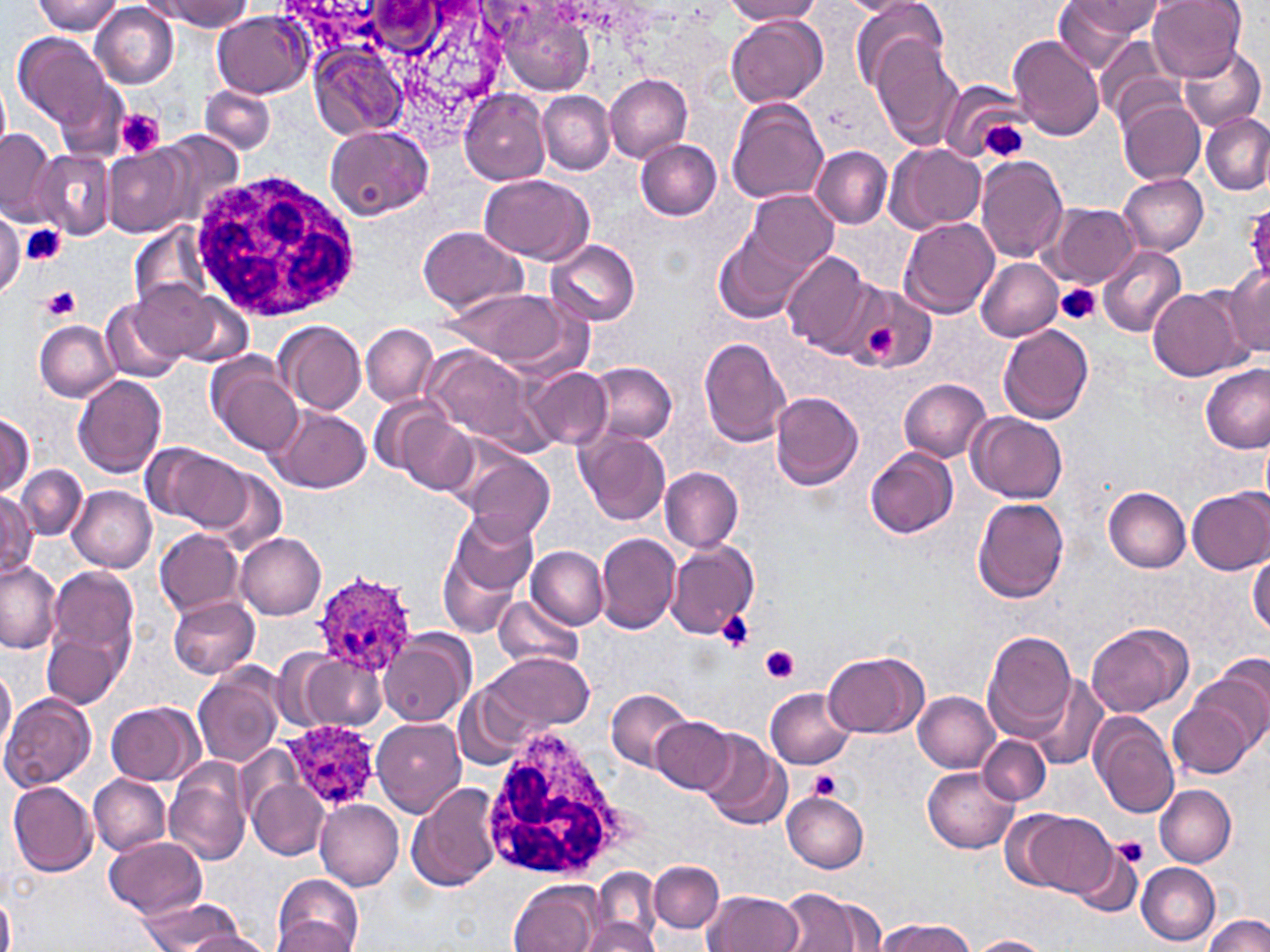 Approximate bounding boxes as (x1, y1, x2, y2) in pixels. Uninfected red blood cell locations: (33, 0, 124, 35), (159, 0, 249, 30), (726, 0, 822, 24), (842, 0, 927, 16), (1053, 0, 1148, 73), (1147, 0, 1248, 79), (89, 2, 178, 88), (1070, 2, 1168, 39), (851, 3, 948, 90), (496, 4, 599, 97), (213, 11, 310, 97), (727, 15, 828, 109), (11, 31, 123, 141), (1094, 34, 1181, 126), (1008, 35, 1105, 142), (873, 36, 964, 149), (309, 44, 407, 142), (1175, 44, 1264, 133), (603, 73, 692, 162), (0, 76, 11, 158), (937, 79, 1026, 162), (201, 84, 275, 154), (459, 89, 550, 186), (537, 90, 615, 175), (727, 98, 830, 205), (1118, 101, 1206, 186), (1201, 111, 1269, 195), (324, 124, 433, 221), (0, 128, 56, 220), (157, 131, 245, 229), (635, 139, 723, 220), (884, 143, 987, 234), (103, 145, 192, 238), (811, 145, 892, 228), (32, 151, 115, 239), (974, 156, 1069, 265), (480, 174, 593, 263), (1119, 174, 1208, 254), (742, 190, 837, 276), (1044, 203, 1139, 287), (1242, 203, 1270, 284), (0, 210, 24, 298), (900, 217, 1000, 317), (130, 224, 215, 312), (418, 225, 527, 313), (715, 231, 810, 324), (546, 238, 640, 326), (1096, 245, 1188, 339), (781, 250, 878, 357), (975, 257, 1064, 341), (1226, 265, 1270, 357), (129, 278, 229, 363), (850, 284, 935, 374), (442, 285, 576, 369), (1147, 285, 1250, 382), (100, 296, 185, 385), (34, 320, 118, 401), (276, 321, 367, 414), (362, 324, 438, 406), (996, 324, 1094, 424), (698, 337, 792, 448), (422, 345, 549, 453), (204, 353, 303, 457), (583, 361, 677, 448), (1199, 362, 1269, 453), (525, 367, 613, 450), (73, 372, 167, 478), (900, 379, 991, 461), (770, 389, 865, 491), (369, 393, 447, 476), (268, 406, 371, 494), (1, 410, 35, 496), (397, 411, 478, 492), (967, 412, 1067, 504), (575, 429, 672, 527), (1260, 431, 1270, 512), (150, 445, 252, 530), (865, 447, 958, 539), (460, 452, 555, 543), (16, 465, 88, 539), (209, 467, 287, 555), (660, 467, 743, 552), (68, 486, 157, 573), (1104, 487, 1192, 573), (1187, 487, 1270, 574), (0, 490, 39, 580), (971, 496, 1070, 604), (452, 512, 540, 595), (154, 528, 243, 616), (596, 532, 683, 634), (235, 533, 327, 619), (665, 540, 759, 640), (438, 542, 525, 638), (528, 546, 607, 628), (1247, 553, 1269, 637), (0, 559, 63, 655), (46, 565, 140, 671), (168, 594, 261, 678), (495, 596, 581, 668), (1086, 622, 1192, 718), (43, 624, 130, 710), (982, 630, 1077, 740), (378, 634, 469, 727), (823, 650, 928, 738), (487, 651, 595, 732), (295, 654, 384, 729), (0, 664, 16, 763), (192, 665, 285, 766), (1193, 665, 1270, 757), (1033, 676, 1108, 770), (453, 681, 537, 771), (766, 686, 857, 769), (608, 689, 694, 771), (914, 692, 1001, 773), (1, 693, 95, 791), (1168, 693, 1258, 779), (106, 700, 201, 785), (1091, 713, 1180, 819), (372, 717, 467, 818), (652, 717, 735, 794), (697, 730, 792, 831), (978, 735, 1051, 805), (235, 746, 301, 825), (164, 759, 252, 866), (922, 767, 1018, 853), (90, 774, 171, 855), (248, 778, 330, 860), (9, 780, 99, 877), (406, 781, 502, 891), (1155, 785, 1237, 866), (781, 792, 869, 872), (315, 800, 404, 891), (1011, 808, 1113, 898), (1111, 833, 1151, 870), (106, 835, 207, 920), (1070, 846, 1142, 918), (649, 860, 723, 933), (1136, 862, 1221, 944), (592, 867, 662, 948), (272, 874, 365, 951), (508, 878, 604, 951), (774, 889, 884, 952), (705, 890, 803, 952), (136, 900, 241, 950), (1202, 914, 1268, 952), (584, 916, 661, 952), (272, 917, 356, 950), (878, 918, 977, 952), (183, 930, 273, 952), (970, 935, 1051, 951). Platelet locations: (116, 109, 164, 159), (980, 120, 1029, 162), (22, 223, 65, 268), (1056, 282, 1101, 327), (41, 287, 82, 322), (865, 329, 902, 359), (717, 610, 755, 652), (761, 646, 800, 683), (806, 770, 844, 801), (1112, 836, 1149, 867). White blood cell locations: (186, 166, 365, 324), (481, 723, 626, 884). Plasmodium ovale-infected red blood cell locations: (312, 566, 420, 673), (276, 719, 379, 812). Slide-level diagnosis: Plasmodium ovale. Image is 1270×952 pixels. Captured at 1000x magnification. One field of a larger specimen. Thin blood smear. May-Grünwald-Giemsa stain. Light microscopy.